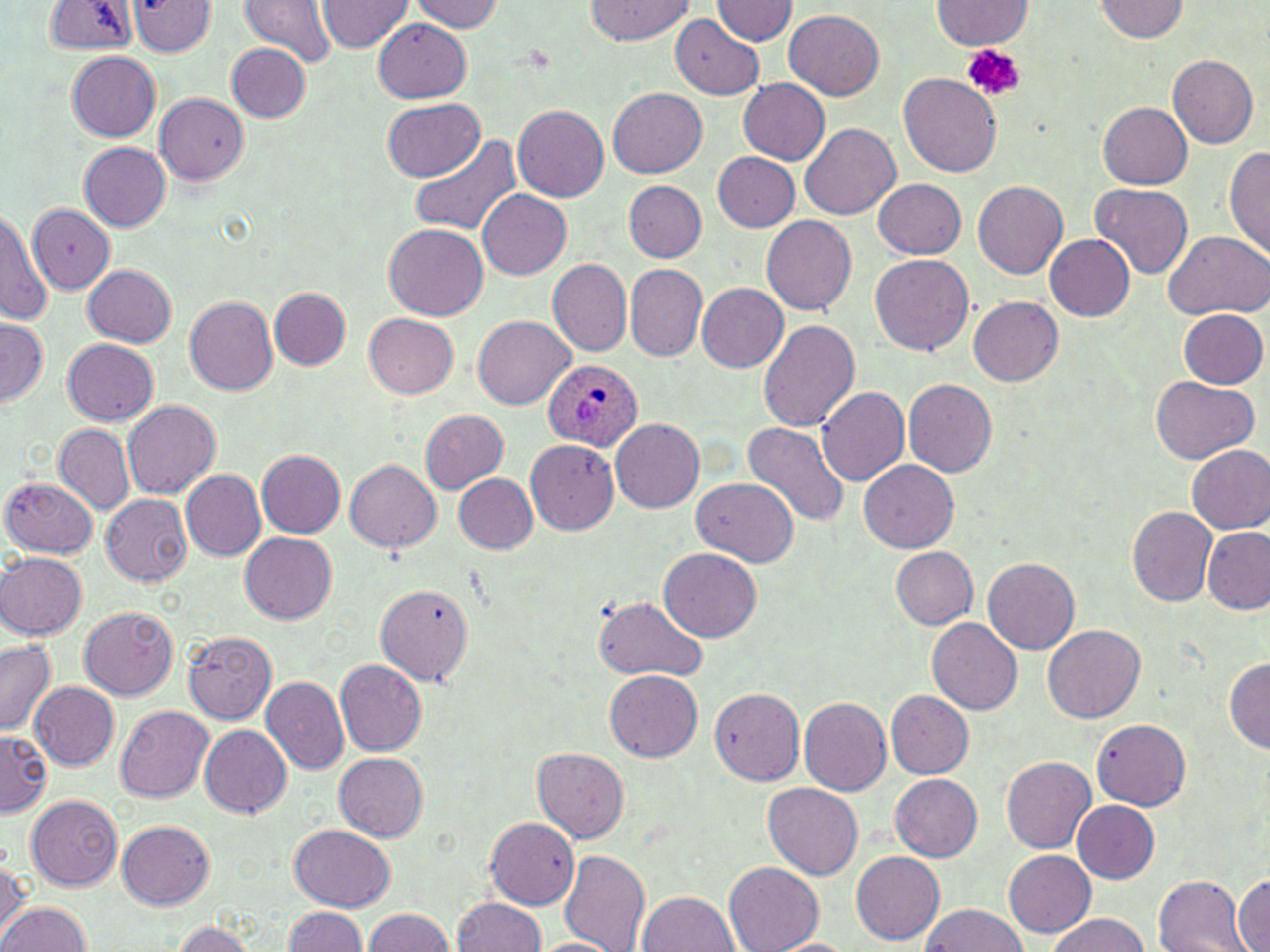 Approximate bounding boxes as [x1, y1, x2, y2] in pixels. Plasmodium ovale-infected red blood cell locations: [546, 359, 646, 450]. Uninfected red blood cell locations: [125, 0, 216, 56], [237, 0, 340, 67], [586, 0, 693, 44], [933, 0, 1033, 49], [1094, 0, 1189, 41], [316, 1, 413, 53], [409, 1, 504, 32], [713, 1, 797, 44], [43, 2, 137, 54], [785, 9, 884, 100], [671, 13, 765, 100], [373, 19, 472, 101], [225, 43, 310, 122], [68, 52, 161, 140], [1167, 55, 1259, 148], [898, 72, 1002, 177], [738, 79, 830, 164], [609, 87, 707, 178], [156, 92, 248, 184], [384, 97, 485, 180], [1099, 102, 1192, 190], [513, 105, 609, 201], [800, 121, 900, 219], [408, 133, 524, 236], [78, 142, 170, 231], [1224, 143, 1270, 262], [711, 153, 799, 231], [873, 178, 966, 259], [623, 181, 707, 261], [973, 181, 1068, 279], [1090, 183, 1194, 278], [478, 188, 572, 279], [29, 203, 115, 292], [0, 208, 51, 326], [760, 215, 858, 313], [385, 224, 489, 322], [1162, 230, 1269, 321], [1044, 235, 1135, 322], [870, 255, 974, 356], [549, 258, 632, 355], [83, 264, 176, 348], [623, 264, 709, 361], [696, 282, 789, 373], [270, 288, 350, 370], [184, 295, 278, 395], [969, 296, 1062, 387], [1178, 309, 1268, 389], [365, 314, 459, 398], [472, 314, 574, 409], [0, 318, 48, 408], [760, 319, 860, 432], [63, 339, 159, 425], [1150, 377, 1258, 463], [904, 378, 997, 477], [818, 386, 910, 485], [123, 399, 220, 498], [421, 409, 509, 494], [611, 419, 704, 512], [743, 420, 849, 530], [54, 424, 134, 515], [525, 438, 620, 535], [1184, 443, 1270, 533], [258, 450, 345, 537], [345, 459, 440, 551], [860, 459, 959, 552], [181, 471, 267, 560], [453, 473, 537, 554], [2, 475, 99, 559], [691, 476, 798, 565], [101, 493, 192, 586], [1127, 507, 1216, 608], [1202, 526, 1269, 614], [240, 532, 337, 624], [661, 547, 760, 641], [890, 547, 978, 629], [1, 553, 87, 639], [983, 559, 1079, 654], [374, 583, 474, 685], [594, 595, 707, 681], [79, 607, 177, 700], [928, 617, 1022, 716], [1043, 623, 1144, 723], [183, 630, 278, 725], [0, 640, 56, 735], [335, 658, 427, 755], [1224, 659, 1269, 751], [605, 670, 702, 762], [262, 676, 349, 773], [28, 680, 119, 769], [710, 686, 806, 785], [887, 690, 973, 780], [799, 696, 891, 796], [116, 704, 214, 803], [1090, 718, 1191, 810], [200, 724, 292, 818], [0, 728, 54, 814], [533, 748, 628, 842], [333, 751, 428, 842], [1001, 756, 1096, 853], [889, 773, 983, 862], [764, 784, 863, 878], [25, 795, 123, 890], [1072, 800, 1159, 883], [485, 817, 580, 909], [118, 820, 214, 909], [290, 823, 396, 911], [559, 848, 651, 952], [851, 850, 943, 943], [1004, 851, 1097, 936], [1, 856, 31, 939], [725, 862, 823, 951], [1233, 874, 1270, 950], [1154, 875, 1251, 952], [641, 891, 738, 951], [453, 896, 546, 951], [0, 901, 92, 952], [920, 903, 1028, 951], [282, 906, 371, 952], [362, 908, 453, 952], [1046, 913, 1150, 952], [169, 920, 257, 952], [530, 937, 621, 952], [768, 938, 858, 952]. Platelet locations: [961, 44, 1024, 100]. Slide-level diagnosis: Plasmodium ovale. Light microscopy. Thin blood smear. One field of a larger specimen. Image is 1270×952 pixels. 1000x magnification. May-Grünwald-Giemsa-stained preparation.